Report the malaria status of this cell.
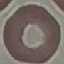

It is uninfected.

capture: smartphone camera at the microscope eyepiece
preparation: thin blood smear
stain: Giemsa
image_type: cell patch, automatically extracted from a larger field of view and resized to 64 × 64 pixels